Name the parasite shown.
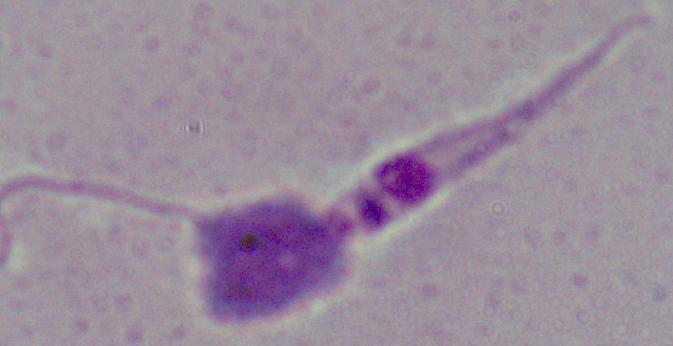

Leishmania.

Summary:
  - Magnification: 1000x
  - Modality: photomicrograph